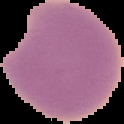

Summary:
  - Preparation: thin blood smear
  - Malaria status: parasitized
  - Image type: cell region segmented out of the field of view; surrounding area masked to black
  - Image size: 124×124 pixels